Report the malaria status of this cell.
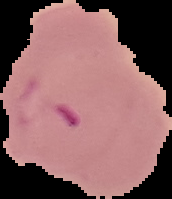
Parasitized.

Summary:
  - Preparation: thin blood film
  - Image size: 172×199 pixels
  - Image type: segmented cell region with the area outside set to black